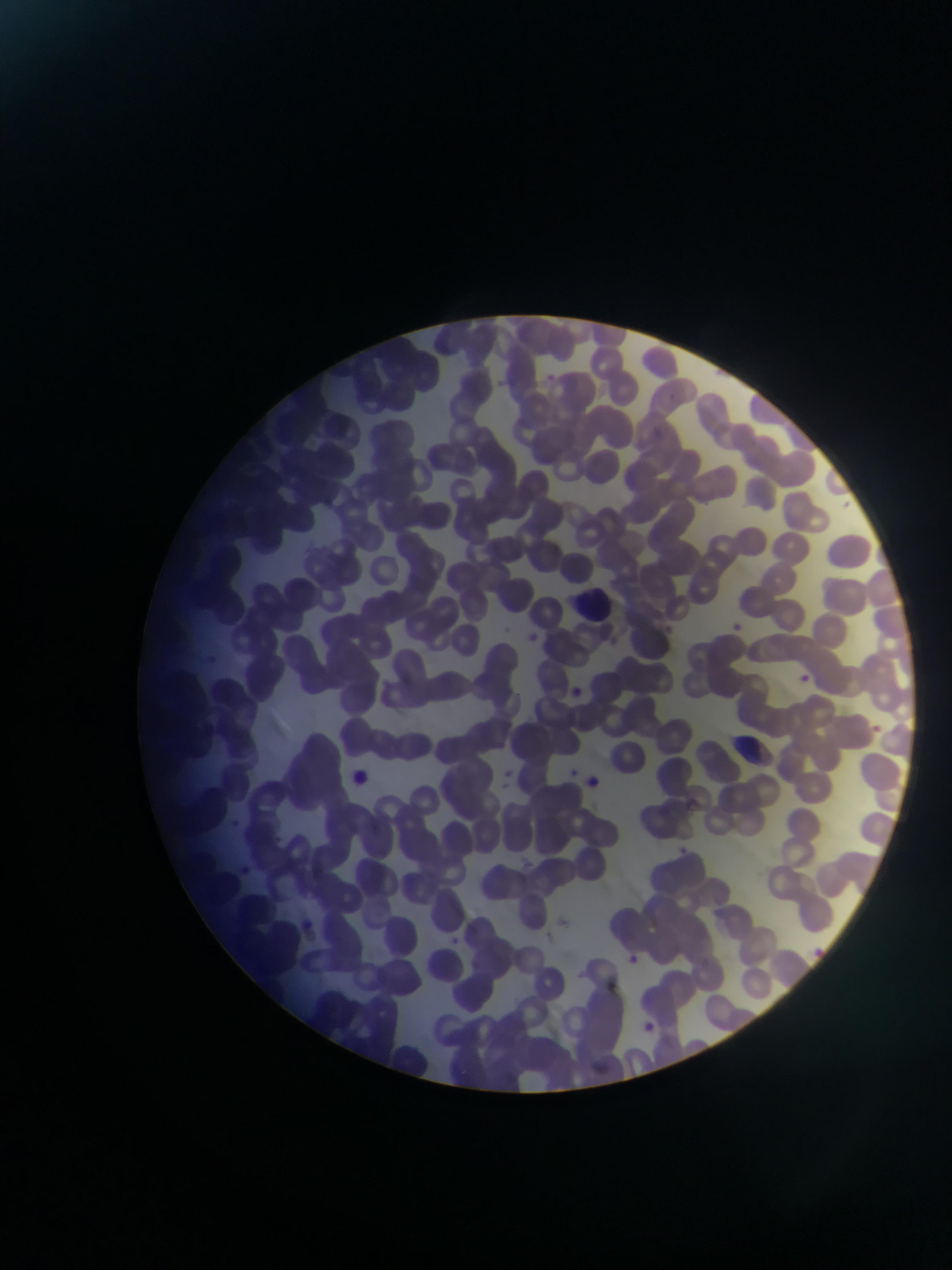
Approximate bounding boxes as (left, top, right, bottom) in pixels.
Summary:
  - Leukocyte locations: (574, 587, 617, 627), (729, 728, 761, 768)
  - Preparation: thin blood smear
  - Image size: 952×1270 pixels
  - Capture: mobile-phone photograph through a microscope
  - Country: Ghana
  - Field of view: single